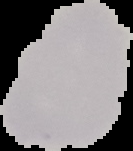
image size = 133×151 pixels
image type = cell region segmented out of the field of view; surrounding area masked to black
result = no malaria parasites seen
preparation = thin blood smear